Give the extent of all Plasmodium ovale-infected red blood cells.
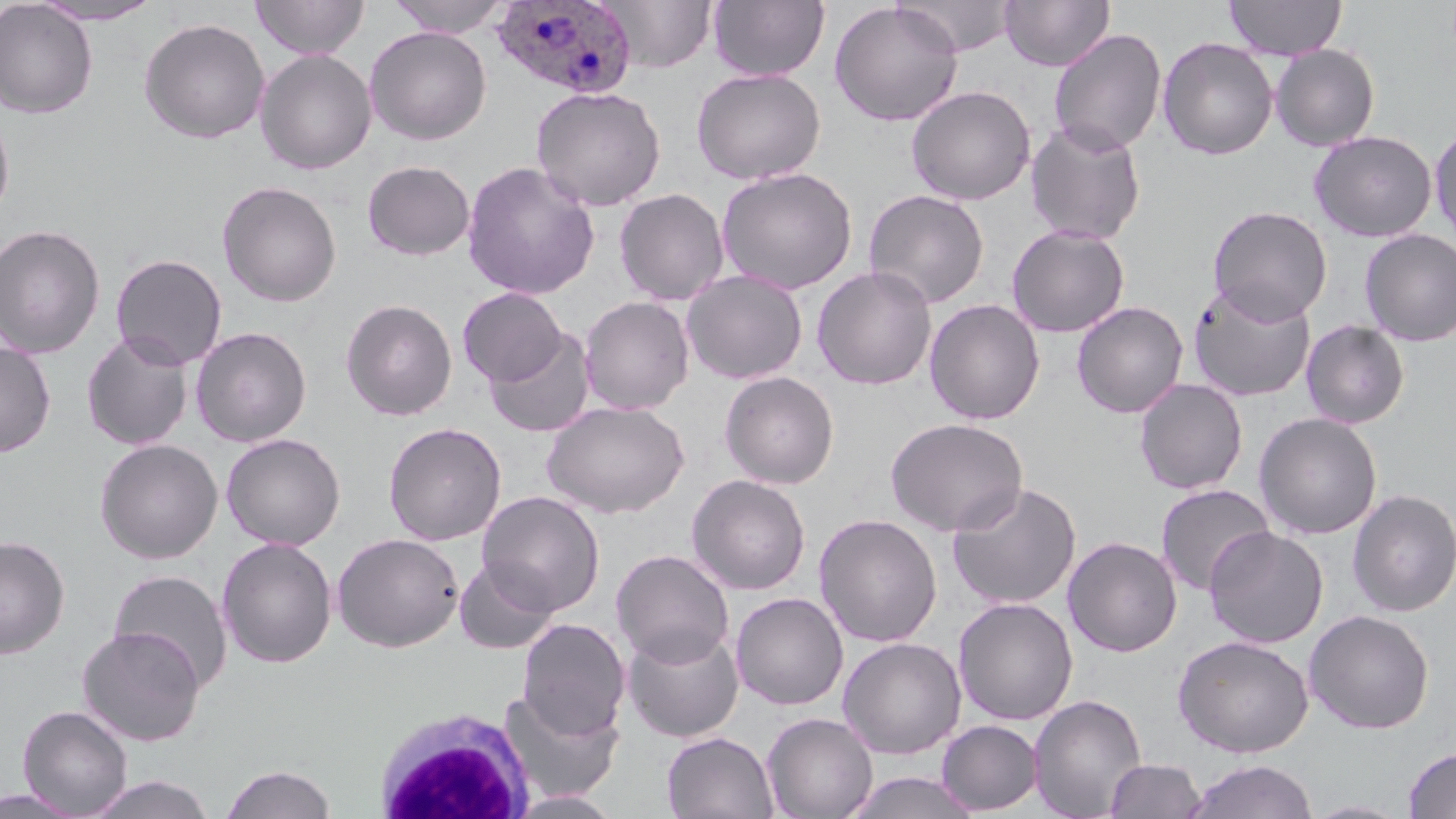

Approximate bounding boxes as named x1/y1/x2/y2 corners in pixels.
Plasmodium ovale-infected red blood cells: (x1=490, y1=1, x2=637, y2=100).

White blood cell locations: (x1=372, y1=708, x2=534, y2=819). Uninfected red blood cell locations: (x1=251, y1=0, x2=369, y2=59), (x1=387, y1=0, x2=513, y2=37), (x1=601, y1=0, x2=716, y2=73), (x1=708, y1=0, x2=829, y2=81), (x1=898, y1=0, x2=1017, y2=55), (x1=1000, y1=0, x2=1115, y2=71), (x1=1224, y1=0, x2=1346, y2=60), (x1=0, y1=1, x2=98, y2=119), (x1=29, y1=1, x2=164, y2=25), (x1=829, y1=1, x2=964, y2=127), (x1=138, y1=17, x2=269, y2=144), (x1=365, y1=26, x2=492, y2=145), (x1=1048, y1=28, x2=1167, y2=155), (x1=1157, y1=37, x2=1278, y2=160), (x1=1270, y1=44, x2=1380, y2=151), (x1=255, y1=49, x2=377, y2=175), (x1=691, y1=67, x2=826, y2=185), (x1=906, y1=85, x2=1035, y2=205), (x1=530, y1=86, x2=666, y2=212), (x1=0, y1=105, x2=15, y2=226), (x1=1025, y1=119, x2=1147, y2=244), (x1=1430, y1=124, x2=1456, y2=247), (x1=1309, y1=130, x2=1437, y2=242), (x1=362, y1=160, x2=475, y2=260), (x1=462, y1=160, x2=600, y2=300), (x1=716, y1=166, x2=858, y2=294), (x1=217, y1=181, x2=341, y2=307), (x1=614, y1=188, x2=729, y2=306), (x1=864, y1=188, x2=989, y2=308), (x1=1207, y1=205, x2=1332, y2=325), (x1=0, y1=224, x2=106, y2=358), (x1=1006, y1=224, x2=1130, y2=337), (x1=1358, y1=229, x2=1456, y2=346), (x1=0, y1=231, x2=227, y2=362), (x1=111, y1=253, x2=227, y2=369), (x1=811, y1=265, x2=938, y2=390), (x1=682, y1=269, x2=808, y2=384), (x1=1188, y1=280, x2=1318, y2=402), (x1=458, y1=287, x2=566, y2=387), (x1=579, y1=296, x2=695, y2=415), (x1=341, y1=298, x2=457, y2=421), (x1=924, y1=299, x2=1046, y2=425), (x1=1072, y1=300, x2=1188, y2=418), (x1=1300, y1=320, x2=1410, y2=429), (x1=190, y1=326, x2=312, y2=447), (x1=484, y1=328, x2=596, y2=438), (x1=81, y1=331, x2=194, y2=451), (x1=0, y1=341, x2=56, y2=457), (x1=719, y1=371, x2=840, y2=489), (x1=1134, y1=378, x2=1248, y2=494), (x1=542, y1=400, x2=689, y2=517), (x1=1254, y1=412, x2=1382, y2=540), (x1=885, y1=417, x2=1028, y2=536), (x1=383, y1=422, x2=506, y2=546), (x1=221, y1=433, x2=345, y2=550), (x1=95, y1=439, x2=223, y2=564), (x1=686, y1=474, x2=811, y2=595), (x1=947, y1=480, x2=1082, y2=609), (x1=1155, y1=483, x2=1275, y2=596), (x1=1348, y1=489, x2=1456, y2=616), (x1=477, y1=491, x2=605, y2=616), (x1=813, y1=513, x2=943, y2=647), (x1=1204, y1=527, x2=1328, y2=648), (x1=331, y1=532, x2=464, y2=652), (x1=0, y1=535, x2=69, y2=660), (x1=217, y1=536, x2=338, y2=669), (x1=1063, y1=536, x2=1182, y2=656), (x1=611, y1=548, x2=735, y2=667), (x1=454, y1=559, x2=559, y2=654), (x1=108, y1=568, x2=234, y2=692), (x1=730, y1=591, x2=849, y2=710), (x1=953, y1=597, x2=1078, y2=726), (x1=1303, y1=609, x2=1435, y2=734), (x1=517, y1=618, x2=630, y2=739), (x1=76, y1=626, x2=205, y2=746), (x1=622, y1=626, x2=744, y2=743), (x1=1173, y1=634, x2=1314, y2=757), (x1=837, y1=637, x2=966, y2=759), (x1=499, y1=689, x2=623, y2=803), (x1=1028, y1=693, x2=1147, y2=819), (x1=17, y1=705, x2=133, y2=817), (x1=762, y1=712, x2=879, y2=819), (x1=937, y1=719, x2=1043, y2=815), (x1=661, y1=731, x2=779, y2=819), (x1=1403, y1=746, x2=1456, y2=818), (x1=1105, y1=759, x2=1205, y2=818), (x1=1183, y1=759, x2=1319, y2=819), (x1=220, y1=763, x2=338, y2=819), (x1=843, y1=771, x2=982, y2=819), (x1=85, y1=775, x2=216, y2=819), (x1=0, y1=787, x2=86, y2=818), (x1=507, y1=790, x2=623, y2=818), (x1=1304, y1=800, x2=1411, y2=818). Slide-level diagnosis: Plasmodium ovale. May-Grünwald-Giemsa-stained preparation. Image is 1456×819 pixels. 1000x magnification. Thin blood film. Optical microscopy. One field of a larger specimen.